Identify the blood parasite species.
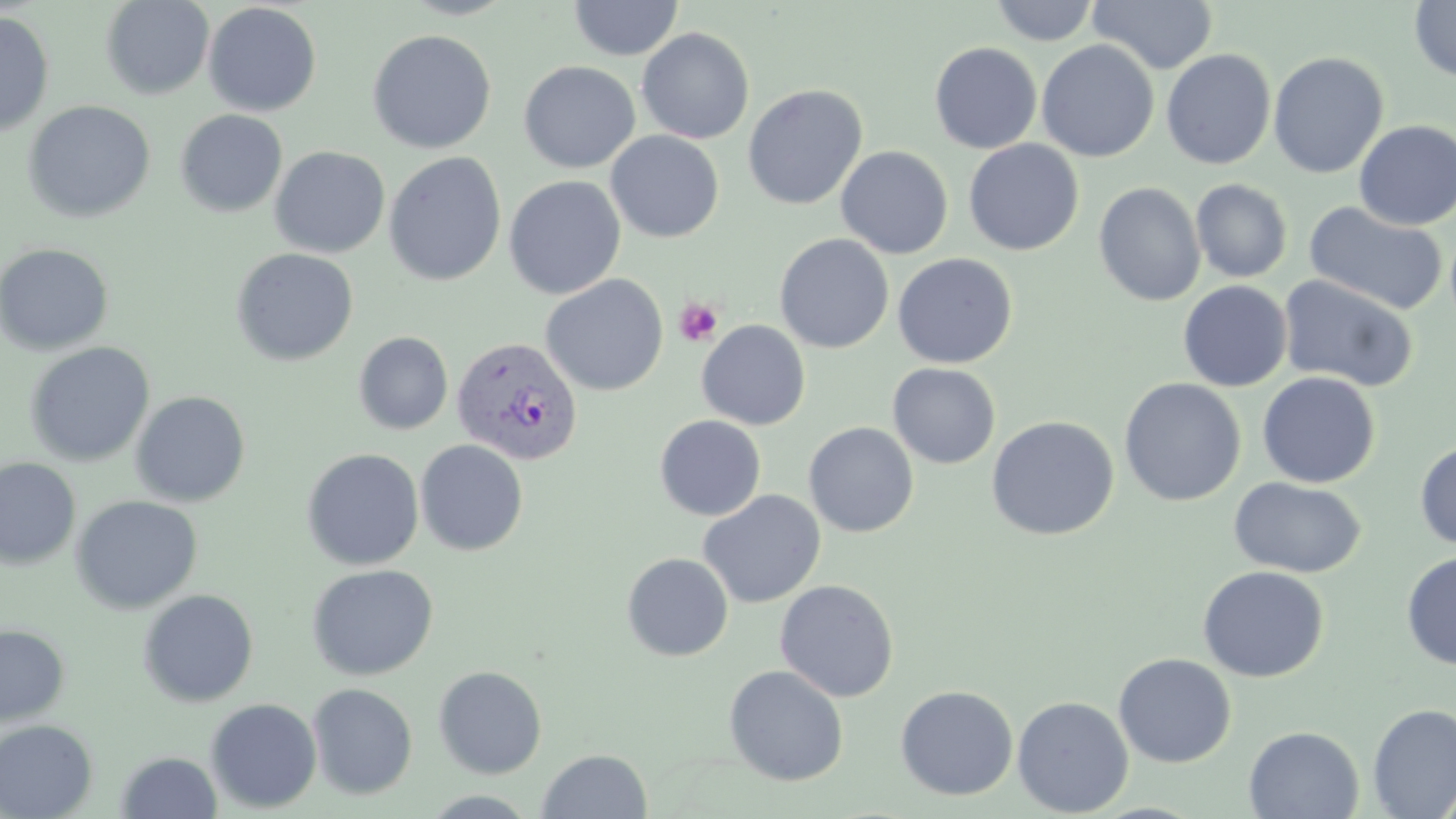

Plasmodium vivax.

field of view = single
Plasmodium vivax-infected red blood cell locations = approximate bounding boxes as (x1,y1)-(x2,y2) corner pairs in pixels: (451,335)-(583,467)
stain = May-Grünwald-Giemsa
platelet locations = approximate bounding boxes as (x1,y1)-(x2,y2) corner pairs in pixels: (673,298)-(722,347)
image size = 1456×819 pixels
magnification = 1000x
uninfected red blood cell locations = approximate bounding boxes as (x1,y1)-(x2,y2) corner pairs in pixels: (101,0)-(214,100), (568,0)-(683,61), (991,0)-(1099,46), (1088,0)-(1217,74), (1408,0)-(1456,82), (202,2)-(322,117), (0,11)-(55,138), (636,27)-(755,144), (367,29)-(496,154), (1036,40)-(1159,162), (929,42)-(1042,154), (1160,49)-(1276,170), (1268,51)-(1389,179), (519,60)-(641,173), (742,84)-(867,210), (22,100)-(156,223), (175,109)-(288,217), (1354,120)-(1456,230), (605,130)-(724,243), (963,139)-(1084,256), (269,146)-(390,258), (836,146)-(953,259), (383,152)-(506,286), (503,175)-(626,299), (1190,178)-(1293,283), (1093,182)-(1205,306), (1305,201)-(1448,316), (774,234)-(894,353), (0,242)-(114,356), (231,247)-(358,366), (892,253)-(1018,369), (540,274)-(668,396), (1278,274)-(1419,393), (1178,280)-(1292,392), (697,320)-(811,430), (354,331)-(453,435), (25,342)-(155,467), (887,362)-(1000,469), (1257,371)-(1380,488), (1119,378)-(1246,507), (130,390)-(251,507), (654,415)-(766,521), (985,415)-(1120,541), (803,422)-(919,537), (415,439)-(529,556), (1415,439)-(1456,549), (302,448)-(424,570), (0,457)-(81,570), (1228,477)-(1366,578), (697,489)-(826,609), (70,495)-(203,615), (1401,551)-(1456,670), (621,553)-(733,661), (307,564)-(438,681), (1198,565)-(1329,682), (775,579)-(899,702), (137,589)-(259,707), (0,623)-(70,727), (1113,653)-(1237,768), (724,664)-(849,786), (433,666)-(547,778), (307,683)-(418,800), (895,685)-(1019,800), (1012,696)-(1133,816), (205,698)-(322,813), (1367,703)-(1456,818), (0,719)-(98,819), (1244,725)-(1364,818), (537,749)-(652,819), (115,751)-(222,818), (420,790)-(542,818)
modality = light microscopy
preparation = thin blood smear